Give the preparation type.
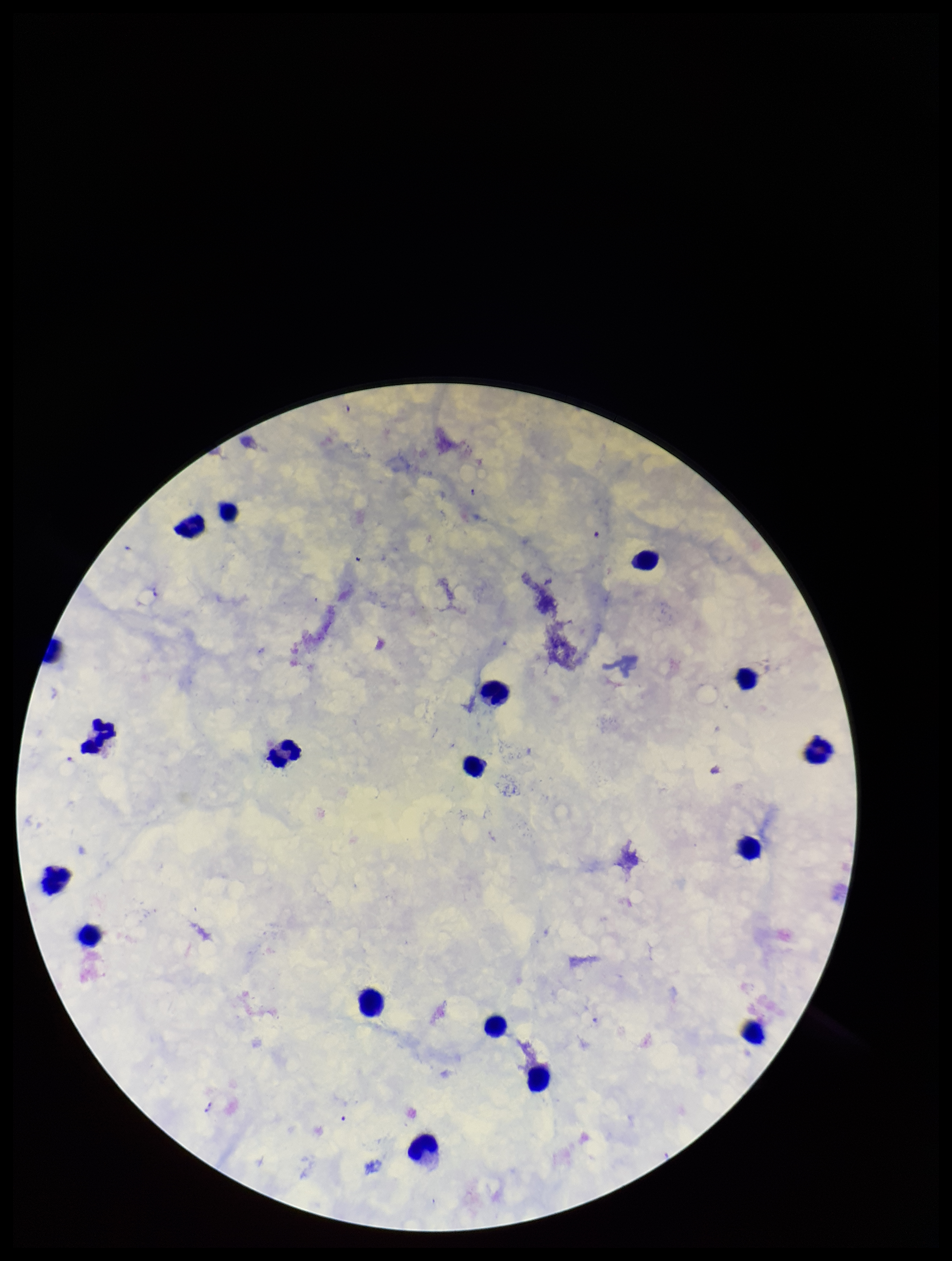

A thick smear.

Photographed through the microscope eyepiece with a smartphone camera. Giemsa stain. Species reported for this patient: Plasmodium falciparum. Parasite count: 0. Plasmodium parasites: none seen. Image is 952×1261 pixels. One field from this slide. Leukocyte count: 19. Patient malaria status: positive.